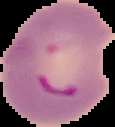

malaria status = parasitized
preparation = thin blood film
image size = 115×127 pixels
image type = segmented cell region with the area outside set to black